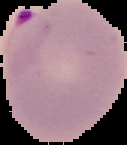
Image is 127×145 pixels. From a thin blood smear. Malaria status: parasitized. Cell region segmented out of the field of view; the surrounding area is masked to black.